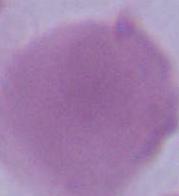

Summary:
  - Modality: photomicrograph
  - Identification: red blood cell
  - Magnification: 1000x